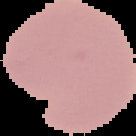

Image is 136×136 pixels. The area outside the segmented cell region is set to black. Malaria status: uninfected. From a thin blood film.